State which parasite is depicted.
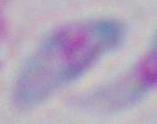
Toxoplasma gondii.

Photomicrograph. 1000x magnification.